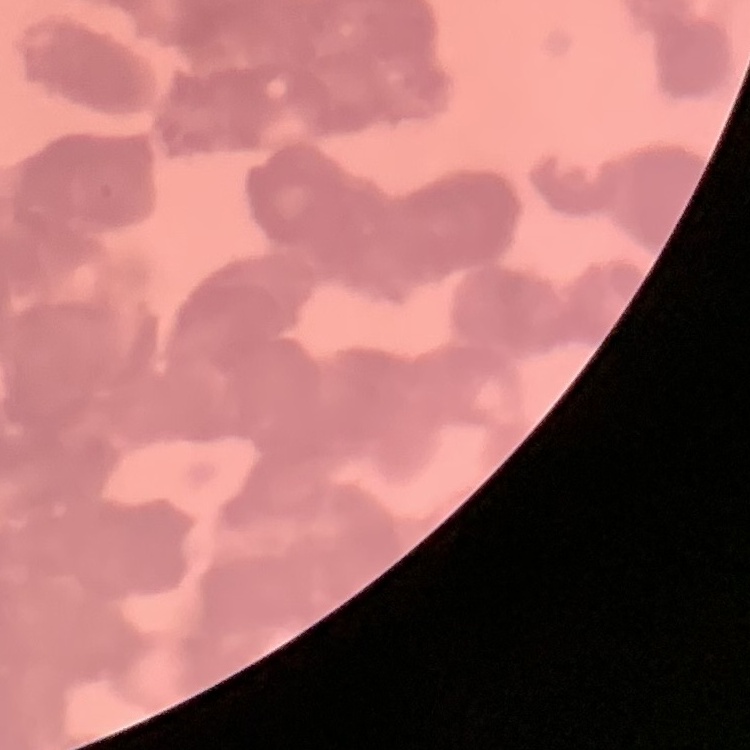
erythrocyte_morphology: rouleaux formation
image_type: square crop of a larger photomicrograph
stain: Field's or Giemsa
preparation: thin blood film